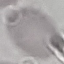
result = negative for malaria parasites
capture = smartphone through the microscope eyepiece
preparation = thin smear
stain = Giemsa
image type = automatically extracted cell patch, resized to 64 × 64 pixels